Give the position of every Plasmodium parasite.
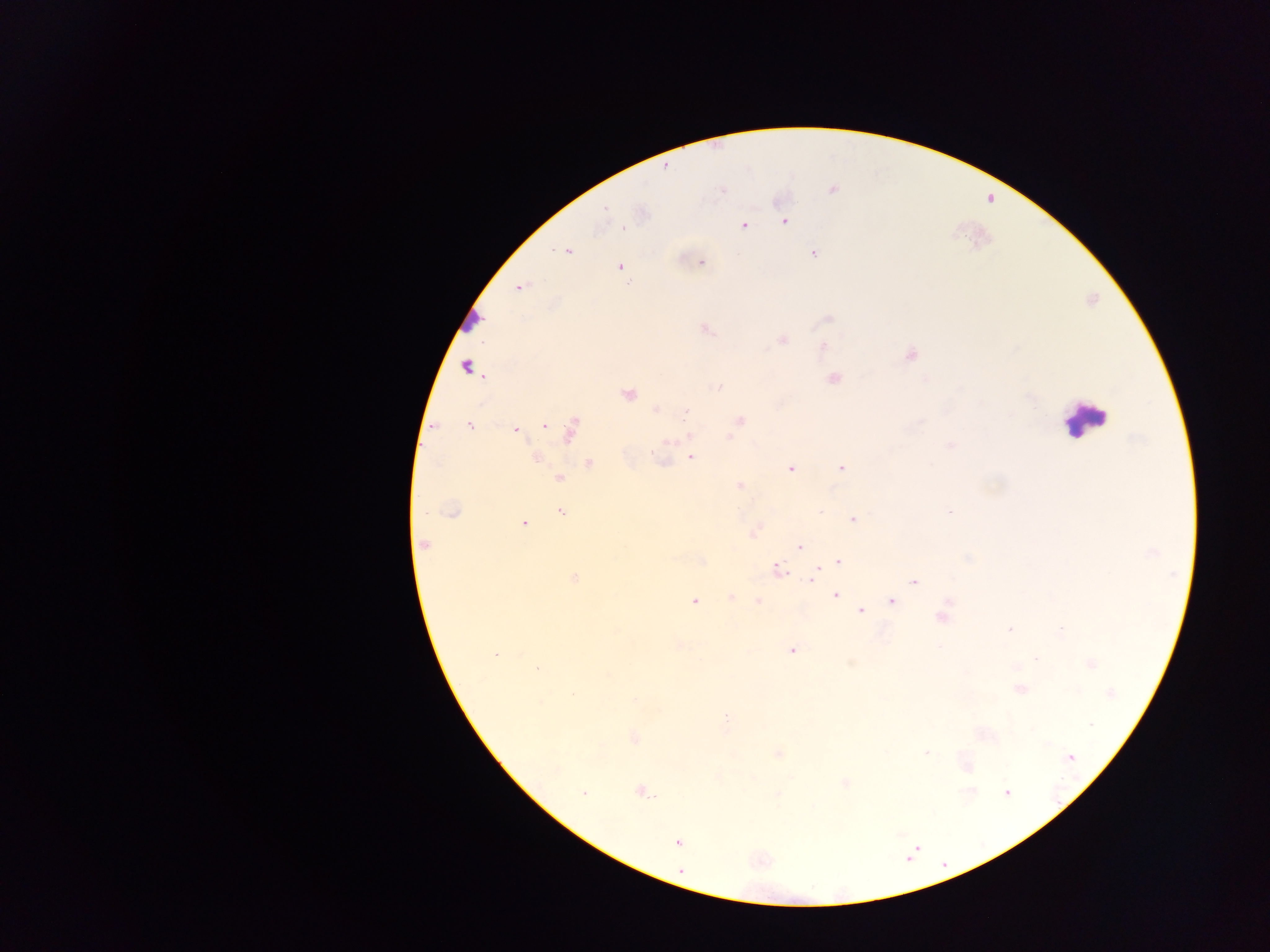
Approximate centers as x y in pixels.
Plasmodium parasites: 665 167; 832 190; 722 191; 606 208; 785 222; 744 225; 624 228; 567 251; 813 254; 701 262; 620 267; 521 287; 828 318; 707 330; 782 339; 823 346; 910 356; 465 366; 833 379; 718 387; 628 394; 655 410; 686 411; 739 420; 469 426; 545 426; 516 429; 570 430; 689 437; 730 437; 950 446; 536 457; 691 458; 589 463; 841 468; 791 469; 559 479; 739 485; 452 512; 560 512; 949 512; 853 519; 524 523; 424 544; 799 547; 838 561; 777 569; 574 578; 812 578; 914 581; 836 595; 731 597; 758 600; 694 601; 891 601; 861 611; 941 618; 1009 628; 1061 630; 792 650; 496 655; 1036 659; 1092 665; 537 668; 1020 690; 635 699; 1090 724; 634 738; 926 753; 779 754; 1070 757; 555 770; 845 783; 641 792; 1006 792; 584 793; 777 795; 678 842.

{
  "preparation": "thick blood smear",
  "capture": "mobile-phone photograph through a microscope",
  "image_size": "1270×952 pixels",
  "country": "Ghana",
  "field_of_view": "single",
  "leukocyte_locations": "approximate centers as x y in pixels: 469 319; 1085 420"
}